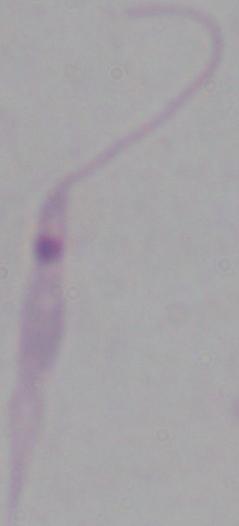 A Leishmania parasite is seen. Micrograph. Captured at 1000x magnification.